Classify this cell by malaria status.
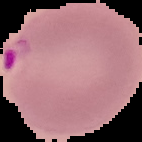

It is parasitized.

Summary:
  - Image size: 142×142 pixels
  - Preparation: thin blood film
  - Image type: cell region segmented out of the field of view; surrounding area masked to black